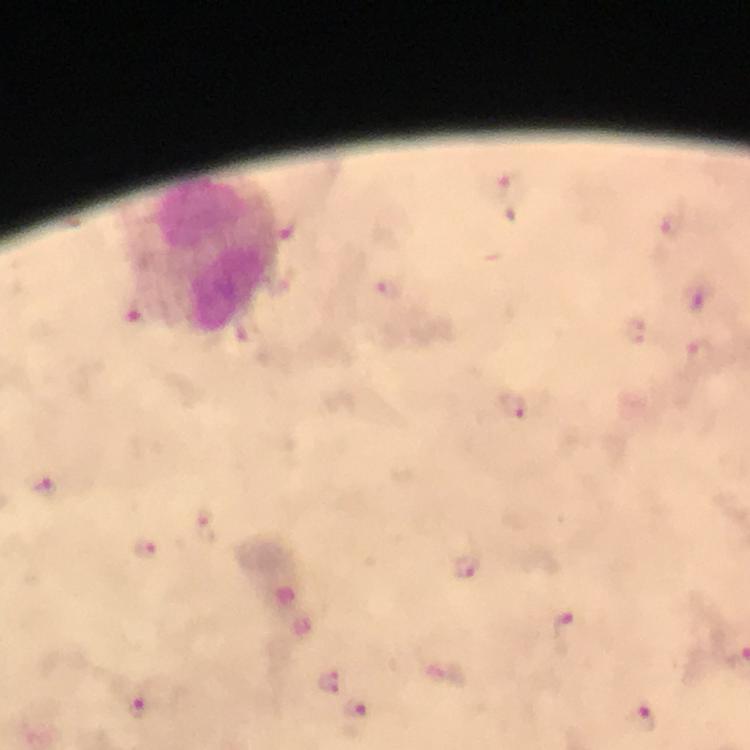 Approximate object centers, in pixels from the top-left corner. Leukocyte locations: (x=213, y=253). Plasmodium parasite locations: (x=511, y=189), (x=672, y=227), (x=389, y=289), (x=699, y=297), (x=634, y=331), (x=702, y=355), (x=510, y=407), (x=44, y=486), (x=206, y=525), (x=145, y=550), (x=465, y=567), (x=569, y=631), (x=328, y=682), (x=138, y=708), (x=643, y=718). Immersion oil applied. From a diagnostic examination for malaria. Photographed through the microscope with a smartphone camera. Image is 750×750 pixels. Giemsa-stained preparation. Cropped region of a single field of view. 100x magnification. Thick smear.